Identify the parasite.
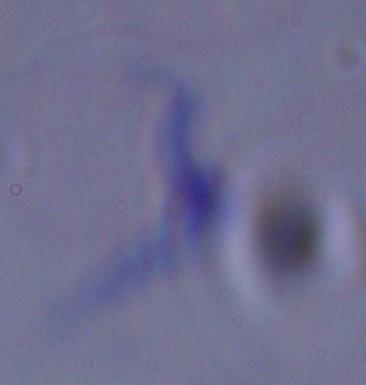
This is a trypanosome.

Photomicrograph. Captured at 1000x magnification.